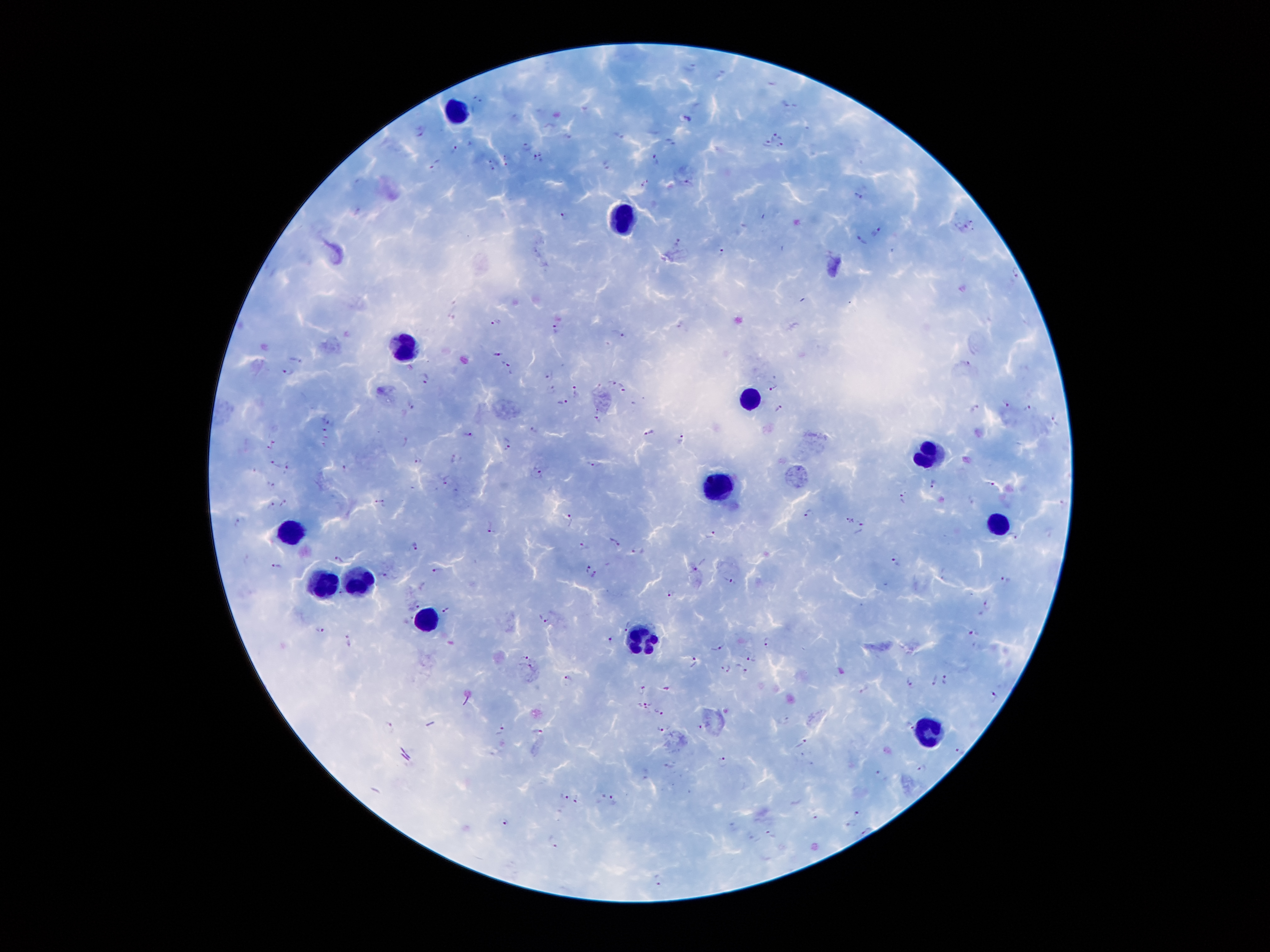
coordinate format = approximate object centers, in pixels from the top-left corner
leukocyte locations = (x=460, y=109), (x=622, y=209), (x=406, y=343), (x=754, y=399), (x=928, y=453), (x=718, y=488), (x=998, y=522), (x=291, y=533), (x=358, y=579), (x=322, y=584), (x=431, y=622), (x=646, y=643), (x=931, y=734)
Plasmodium parasite locations = (x=691, y=66), (x=719, y=73), (x=773, y=83), (x=479, y=99), (x=788, y=104), (x=689, y=118), (x=422, y=131), (x=618, y=134), (x=776, y=135), (x=669, y=141), (x=527, y=144), (x=767, y=144), (x=782, y=146), (x=455, y=149), (x=538, y=156), (x=655, y=159), (x=435, y=161), (x=494, y=161), (x=506, y=161), (x=607, y=162), (x=647, y=182), (x=688, y=182), (x=858, y=196), (x=563, y=215), (x=971, y=222), (x=964, y=227), (x=878, y=231), (x=678, y=239), (x=862, y=239), (x=721, y=250), (x=1015, y=270), (x=497, y=321), (x=557, y=327), (x=620, y=333), (x=497, y=353), (x=297, y=360), (x=506, y=363), (x=967, y=364), (x=287, y=371), (x=548, y=376), (x=425, y=379), (x=612, y=381), (x=623, y=386), (x=773, y=386), (x=551, y=389), (x=573, y=389), (x=563, y=402), (x=1006, y=403), (x=411, y=406), (x=1028, y=407), (x=779, y=408), (x=976, y=408), (x=1053, y=417), (x=330, y=420), (x=598, y=422), (x=533, y=430), (x=650, y=432), (x=326, y=433), (x=467, y=435), (x=683, y=440), (x=405, y=441), (x=507, y=443), (x=272, y=446), (x=323, y=446), (x=455, y=458), (x=418, y=460), (x=274, y=463), (x=593, y=464), (x=287, y=467), (x=345, y=467), (x=538, y=470), (x=447, y=479), (x=935, y=482), (x=272, y=484), (x=989, y=484), (x=902, y=499), (x=379, y=503), (x=286, y=504), (x=271, y=506), (x=807, y=513), (x=569, y=519), (x=850, y=519), (x=239, y=522), (x=490, y=524), (x=861, y=528), (x=710, y=534), (x=1013, y=536), (x=614, y=541), (x=414, y=546), (x=584, y=547), (x=636, y=551), (x=336, y=557), (x=895, y=561), (x=276, y=565), (x=587, y=566), (x=700, y=566), (x=435, y=569), (x=388, y=575), (x=593, y=575), (x=731, y=579), (x=1006, y=579), (x=943, y=580), (x=342, y=592), (x=671, y=593), (x=986, y=603), (x=417, y=605), (x=444, y=612), (x=546, y=620), (x=626, y=627), (x=320, y=629), (x=975, y=633), (x=611, y=639), (x=767, y=642), (x=348, y=643), (x=718, y=648), (x=753, y=659), (x=526, y=660), (x=693, y=662), (x=727, y=669), (x=740, y=669), (x=569, y=679), (x=944, y=679), (x=935, y=680), (x=910, y=681), (x=665, y=688), (x=642, y=690), (x=996, y=698), (x=645, y=704), (x=659, y=712), (x=909, y=725), (x=698, y=726), (x=389, y=727), (x=501, y=730), (x=659, y=730), (x=537, y=731), (x=803, y=743), (x=961, y=750), (x=723, y=760), (x=669, y=765), (x=923, y=769), (x=880, y=775), (x=564, y=794), (x=599, y=798), (x=577, y=800), (x=614, y=801), (x=857, y=813), (x=813, y=819), (x=507, y=821), (x=850, y=824), (x=865, y=829), (x=769, y=835), (x=555, y=841), (x=657, y=880)
patient malaria status = infected with Plasmodium falciparum
field of view = single
image size = 1270×952 pixels
magnification = 100x
preparation = thick blood smear
stain = Giemsa
capture = smartphone camera through the microscope eyepiece